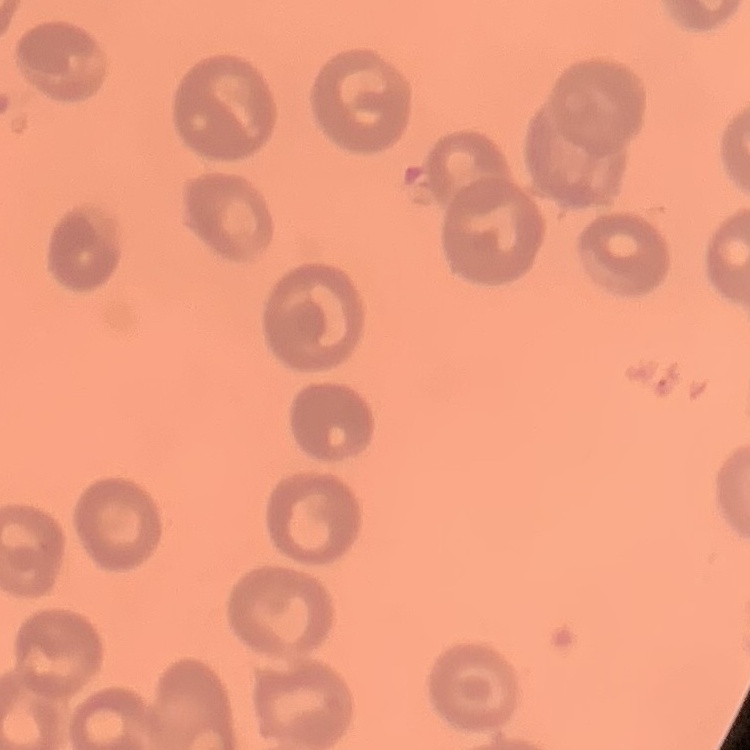

red blood cell morphology = no rouleaux formation
stain = Field's or Giemsa
preparation = thin blood smear
image type = square crop of a larger photomicrograph